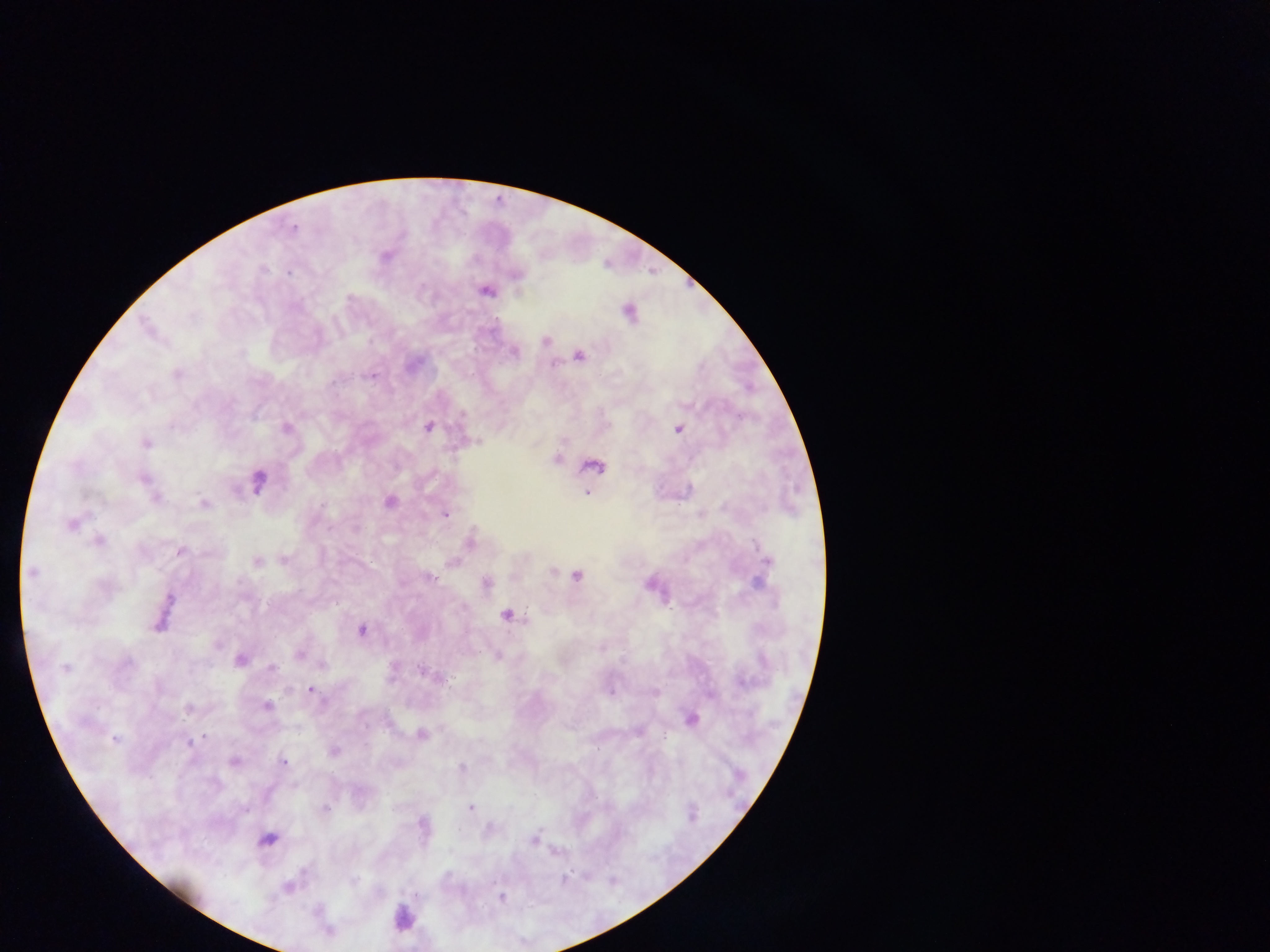
Approximate centers as [x, y] in pixels.
Summary:
  - Plasmodium parasite locations: [293, 228], [385, 257], [264, 270], [290, 273], [516, 275], [486, 291], [629, 313], [545, 341], [514, 353], [578, 356], [177, 373], [372, 375], [332, 382], [462, 415], [428, 427], [286, 429], [678, 429], [146, 443], [557, 459], [593, 467], [144, 479], [258, 482], [586, 493], [154, 497], [390, 501], [203, 503], [322, 505], [446, 514], [71, 524], [470, 540], [98, 541], [758, 543], [180, 551], [284, 560], [257, 561], [766, 561], [452, 562], [552, 571], [32, 572], [576, 576], [429, 578], [486, 583], [758, 583], [169, 600], [507, 615], [160, 623], [361, 630], [299, 655], [497, 656], [241, 660], [127, 664], [322, 664], [65, 668], [272, 669], [423, 672], [742, 682], [311, 690], [654, 692], [267, 706], [188, 708], [692, 719], [421, 734], [204, 736], [665, 736], [115, 739], [188, 744], [335, 752], [234, 762], [284, 762], [462, 768], [470, 808], [245, 809], [323, 809], [692, 815], [421, 824], [488, 828], [268, 839], [533, 840], [554, 853], [564, 879], [353, 881], [288, 888], [502, 897]
  - Leukocyte locations: [404, 918]
  - Country: Ghana
  - Field of view: single
  - Preparation: thick blood film
  - Image size: 1270×952 pixels
  - Capture: mobile-phone photograph through a microscope